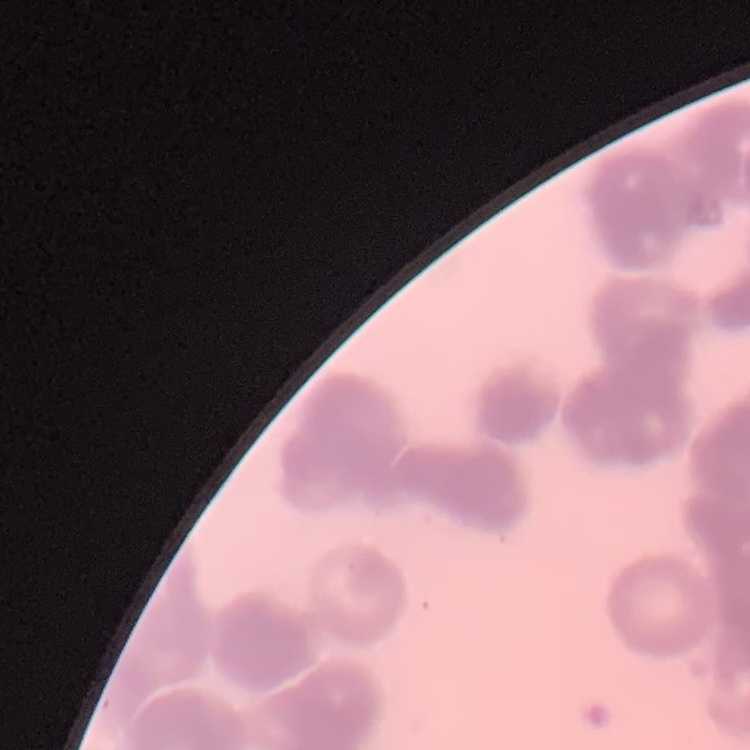 The red blood cells show rouleaux formation. Thin peripheral smear. Stained with either Field's or Giemsa. Square crop of a larger photomicrograph.